State which cell type is depicted.
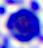
This is a leukocyte.

Summary:
  - Modality: micrograph
  - Magnification: 400x